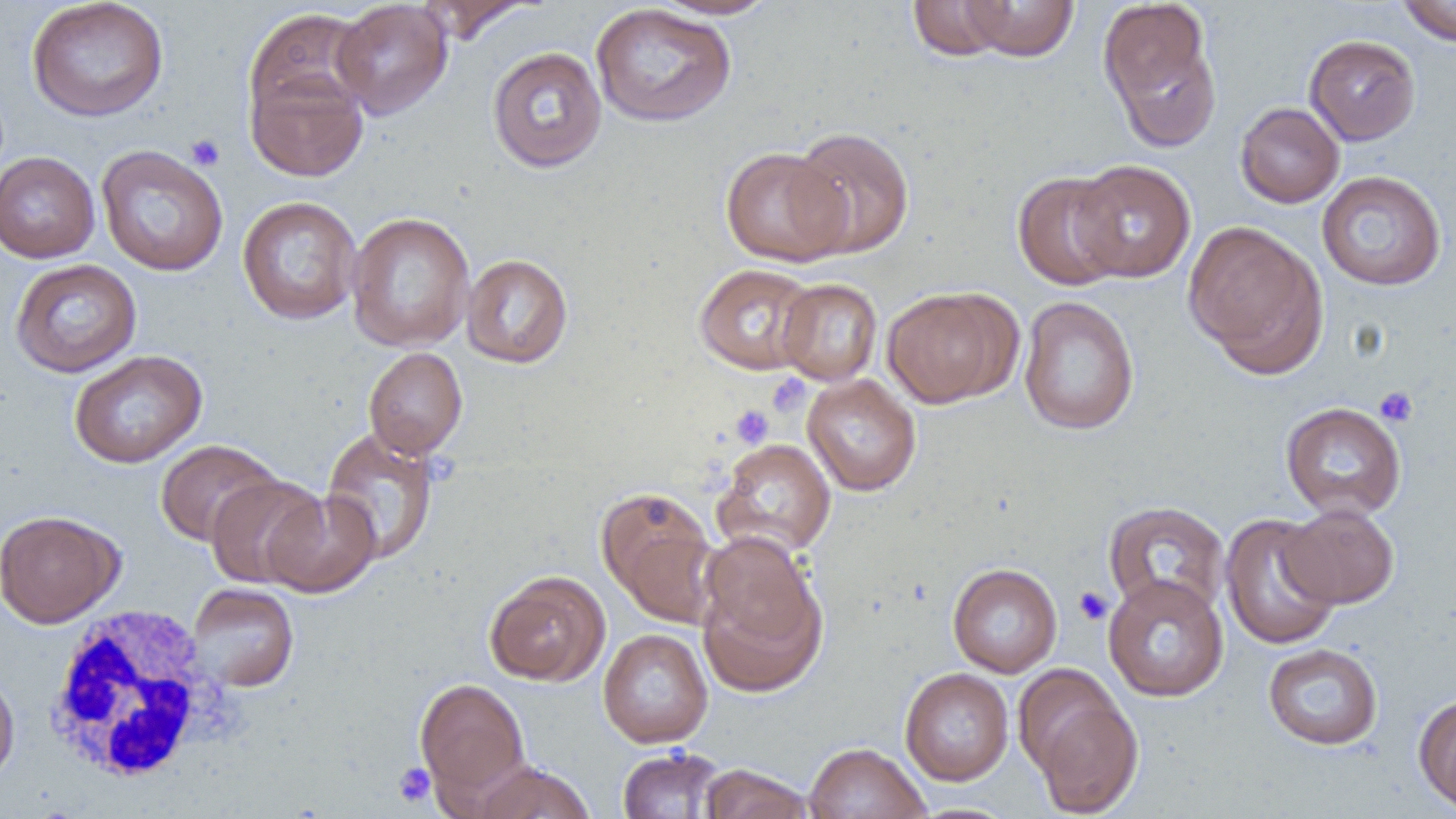
Summary:
  - Coordinate format: approximate bounding boxes as named x1/y1/x2/y2 corners in pixels
  - Uninfected red blood cell locations: (x1=26, y1=0, x2=169, y2=123), (x1=415, y1=0, x2=535, y2=43), (x1=650, y1=0, x2=781, y2=20), (x1=907, y1=0, x2=1014, y2=61), (x1=1395, y1=0, x2=1456, y2=46), (x1=331, y1=1, x2=453, y2=120), (x1=961, y1=1, x2=1080, y2=61), (x1=1098, y1=1, x2=1222, y2=151), (x1=590, y1=3, x2=737, y2=128), (x1=243, y1=8, x2=372, y2=126), (x1=1304, y1=34, x2=1421, y2=145), (x1=487, y1=46, x2=607, y2=173), (x1=246, y1=66, x2=369, y2=182), (x1=1235, y1=102, x2=1344, y2=208), (x1=788, y1=126, x2=915, y2=258), (x1=96, y1=144, x2=229, y2=277), (x1=719, y1=146, x2=851, y2=267), (x1=0, y1=151, x2=101, y2=263), (x1=1069, y1=159, x2=1196, y2=283), (x1=1012, y1=170, x2=1129, y2=291), (x1=1316, y1=171, x2=1447, y2=291), (x1=237, y1=196, x2=362, y2=324), (x1=346, y1=211, x2=475, y2=352), (x1=1183, y1=221, x2=1328, y2=376), (x1=461, y1=253, x2=574, y2=368), (x1=10, y1=258, x2=142, y2=378), (x1=694, y1=263, x2=819, y2=375), (x1=777, y1=278, x2=882, y2=385), (x1=882, y1=287, x2=1016, y2=408), (x1=1018, y1=296, x2=1140, y2=436), (x1=363, y1=347, x2=467, y2=458), (x1=68, y1=350, x2=207, y2=468), (x1=802, y1=374, x2=922, y2=496), (x1=1280, y1=401, x2=1407, y2=520), (x1=321, y1=427, x2=440, y2=566), (x1=711, y1=438, x2=837, y2=560), (x1=155, y1=439, x2=282, y2=547), (x1=205, y1=473, x2=327, y2=590), (x1=596, y1=486, x2=721, y2=626), (x1=262, y1=490, x2=381, y2=598), (x1=1103, y1=500, x2=1230, y2=619), (x1=1280, y1=503, x2=1399, y2=608), (x1=0, y1=509, x2=124, y2=628), (x1=1219, y1=514, x2=1341, y2=651), (x1=695, y1=538, x2=828, y2=697), (x1=947, y1=563, x2=1062, y2=677), (x1=484, y1=570, x2=610, y2=686), (x1=1103, y1=574, x2=1229, y2=702), (x1=187, y1=582, x2=299, y2=692), (x1=598, y1=629, x2=713, y2=748), (x1=1262, y1=643, x2=1383, y2=750), (x1=900, y1=667, x2=1014, y2=786), (x1=0, y1=669, x2=20, y2=787), (x1=414, y1=676, x2=531, y2=803), (x1=1028, y1=687, x2=1145, y2=818), (x1=1413, y1=692, x2=1456, y2=814), (x1=804, y1=742, x2=930, y2=819), (x1=616, y1=747, x2=728, y2=818), (x1=469, y1=760, x2=597, y2=819), (x1=698, y1=763, x2=816, y2=819)
  - Platelet locations: (x1=186, y1=133, x2=225, y2=171), (x1=766, y1=373, x2=811, y2=417), (x1=1375, y1=386, x2=1419, y2=428), (x1=730, y1=405, x2=774, y2=448), (x1=1073, y1=586, x2=1113, y2=625), (x1=393, y1=762, x2=436, y2=807)
  - White blood cell locations: (x1=41, y1=605, x2=236, y2=786)
  - Slide-level diagnosis: negative for blood parasites
  - Modality: light microscopy
  - Magnification: 1000x
  - Image size: 1456×819 pixels
  - Preparation: thin blood smear
  - Field of view: one of a larger specimen